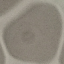 Malaria status: uninfected. Cell patch, automatically extracted from a larger field of view and resized to 64 × 64 pixels. Thin blood film. Photographed with a smartphone camera at the microscope eyepiece. Giemsa stain.